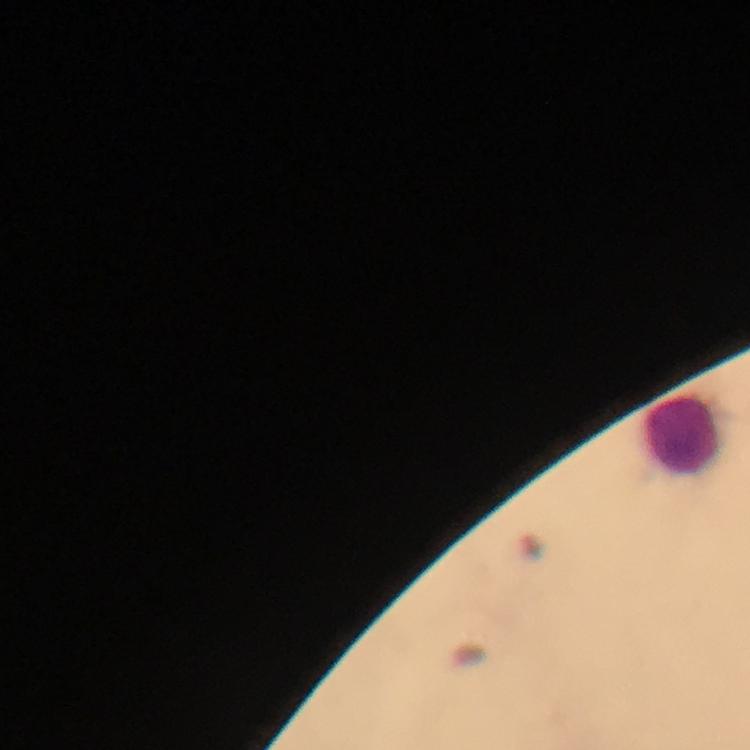

Approximate centers as (x, y) in pixels.
Summary:
  - Leukocyte locations: (682, 436)
  - Cropped from: a single field of view
  - Plasmodium parasites: none seen
  - Immersion oil: applied
  - Stain: Giemsa
  - Magnification: 100x
  - Capture: smartphone mounted on the microscope
  - Image size: 750×750 pixels
  - Preparation: thick blood film
  - Context: from a diagnostic examination for malaria